Identify the parasite.
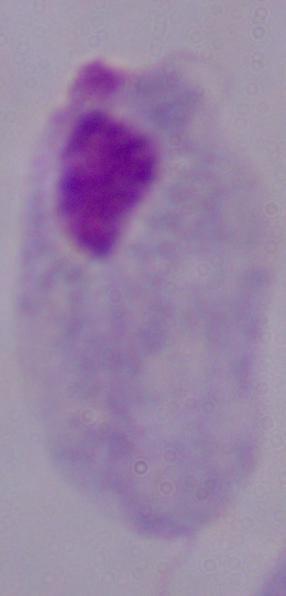

A trichomonad.

Summary:
  - Modality: micrograph
  - Magnification: 1000x